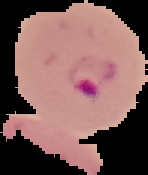 Result: Plasmodium parasites identified. Segmented cell region on a black background. Image is 148×175 pixels. From a thin blood smear.